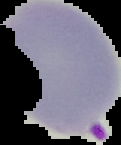 Image is 121×145 pixels. Result: malaria parasites identified. From a thin blood film. Cell region segmented out of the field of view; the surrounding area is masked to black.